Name the blood parasite species.
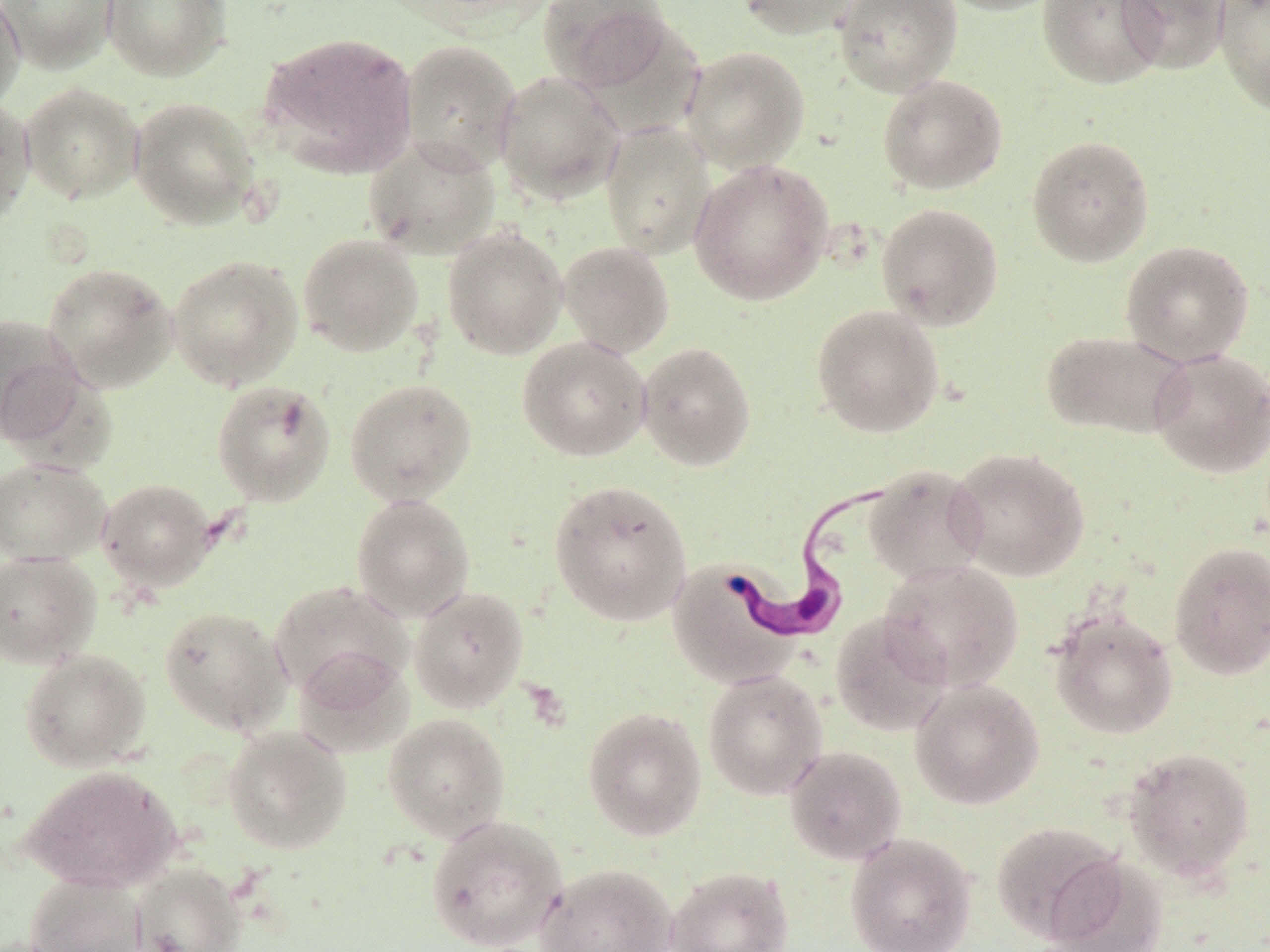
Trypanosoma brucei.

Summary:
  - Coordinate format: approximate bounding boxes as (x1,y1)-(x2,y2) corner pairs in pixels
  - Uninfected red blood cell locations: (0,0)-(118,73), (0,0)-(26,114), (102,0)-(231,81), (539,0)-(674,92), (735,0)-(863,39), (833,0)-(962,97), (935,0)-(1068,16), (1037,0)-(1165,90), (1116,0)-(1230,74), (1214,0)-(1270,116), (259,31)-(419,177), (399,39)-(522,174), (680,46)-(809,172), (493,71)-(625,204), (876,74)-(1009,194), (20,82)-(144,204), (0,96)-(36,228), (129,96)-(261,229), (600,121)-(717,259), (1026,134)-(1155,267), (363,136)-(501,260), (688,158)-(834,306), (876,202)-(1005,331), (442,225)-(568,359), (297,234)-(425,357), (1120,239)-(1255,367), (558,241)-(675,358), (167,254)-(304,390), (43,262)-(179,393), (811,304)-(945,437), (0,313)-(85,447), (1041,329)-(1192,440), (517,336)-(652,462), (636,341)-(757,472), (1149,348)-(1270,478), (344,377)-(478,506), (211,379)-(336,506), (948,446)-(1091,582), (0,457)-(110,566), (863,465)-(989,585), (0,466)-(219,573), (96,478)-(217,591), (548,478)-(693,626), (351,494)-(476,620), (1168,541)-(1270,680), (0,551)-(101,668), (666,559)-(799,688), (879,559)-(1024,691), (268,580)-(412,701), (409,586)-(529,712), (158,605)-(293,736), (1048,611)-(1178,739), (830,612)-(952,736), (19,648)-(151,772), (293,648)-(414,758), (702,668)-(828,800), (910,678)-(1044,810), (583,706)-(707,841), (383,713)-(510,842), (223,725)-(352,854), (784,745)-(906,864), (1122,746)-(1256,880), (20,765)-(181,893), (425,813)-(568,951), (991,820)-(1124,944), (844,833)-(977,952), (1042,853)-(1167,952), (130,862)-(246,952), (536,863)-(678,952), (665,865)-(794,952), (26,873)-(147,952)
  - Trypanosoma brucei locations: (718,471)-(901,644)
  - Image size: 1270×952 pixels
  - Magnification: 1000x
  - Preparation: thin blood film
  - Field of view: one of a larger specimen
  - Stain: May-Grünwald-Giemsa
  - Modality: light microscopy